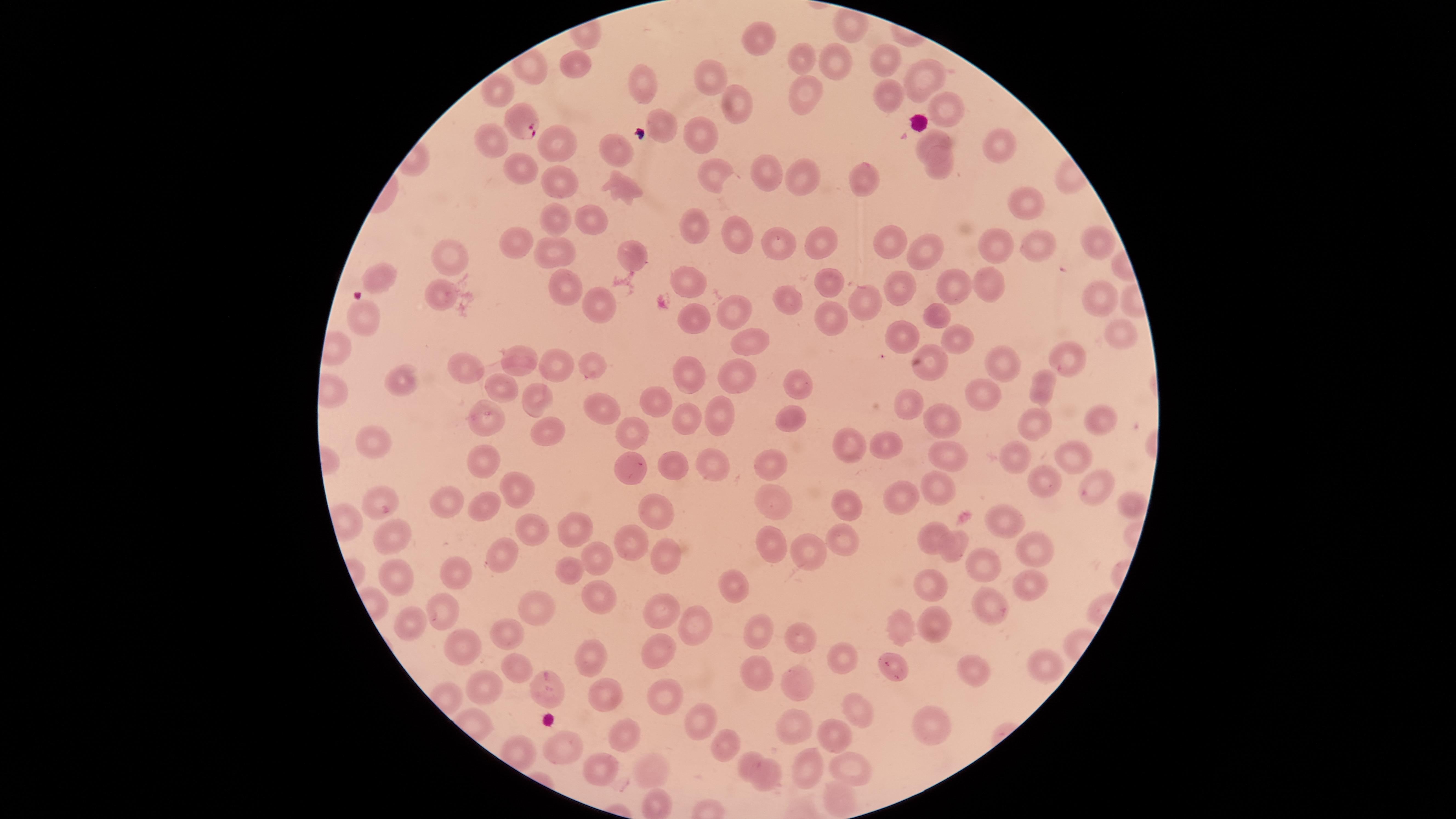 Approximate marker points as [x, y] in pixels. Parasitized red blood cells: [519, 118]. Uninfected red blood cells: [852, 29], [754, 39], [577, 56], [807, 59], [887, 59], [527, 65], [833, 65], [925, 78], [708, 79], [643, 80], [492, 89], [806, 94], [883, 97], [736, 102], [949, 110], [655, 129], [705, 135], [931, 136], [555, 142], [493, 144], [614, 147], [1001, 147], [941, 165], [512, 168], [764, 171], [712, 172], [804, 172], [556, 179], [869, 183], [621, 184], [1029, 205], [558, 220], [598, 220], [694, 232], [508, 239], [783, 240], [736, 241], [1095, 241], [823, 242], [891, 243], [994, 244], [1041, 246], [625, 249], [451, 250], [558, 250], [921, 250], [380, 272], [830, 278], [950, 280], [558, 281], [687, 281], [997, 283], [903, 289], [438, 293], [1099, 293], [780, 294], [868, 298], [602, 299], [726, 309], [937, 314], [359, 318], [687, 321], [836, 322], [1127, 329], [897, 335], [958, 339], [746, 343], [1066, 353], [521, 363], [560, 363], [933, 364], [595, 367], [736, 369], [1005, 369], [468, 370], [691, 374], [403, 378], [799, 378], [501, 387], [1044, 388], [976, 391], [540, 399], [911, 401], [653, 403], [603, 405], [723, 412], [791, 414], [483, 415], [684, 418], [939, 418], [1103, 418], [1038, 425], [634, 429], [546, 432], [380, 440], [851, 444], [889, 446], [1077, 451], [942, 455], [479, 456], [711, 458], [1021, 459], [667, 461], [627, 464], [768, 468], [1033, 477], [1087, 486], [938, 487], [518, 488], [780, 493], [448, 494], [893, 497], [380, 498], [1131, 498], [478, 503], [846, 507], [659, 509], [993, 517], [577, 525], [933, 527], [534, 528], [845, 532], [387, 533], [767, 534], [628, 539], [949, 544], [1028, 545], [805, 548], [502, 551], [665, 552], [591, 557], [570, 565], [980, 565], [393, 567], [460, 571], [932, 579], [736, 584], [1028, 589], [600, 591], [660, 606], [990, 606], [541, 608], [445, 610], [415, 618], [686, 619], [903, 625], [759, 626], [935, 626], [512, 627], [796, 636], [471, 641], [837, 648], [665, 650], [1043, 659], [592, 660], [518, 666], [761, 669], [976, 670], [893, 672], [487, 683], [805, 684], [550, 687], [662, 692], [607, 694], [854, 705], [692, 717], [793, 722], [620, 727], [941, 728], [835, 735], [726, 740], [563, 748], [754, 756], [606, 768], [653, 769], [812, 770], [851, 770], [766, 776], [658, 800], [842, 800]. Photographed with a smartphone camera through the microscope eyepiece. Image is 1456×819 pixels. Giemsa-stained preparation. Single field of view. Presence: malaria parasites detected. Thin blood film. Circular visible region. Species: Plasmodium falciparum.